State which parasite is depicted.
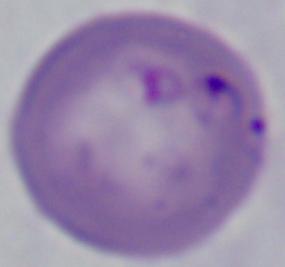
Babesia.

Micrograph. 1000x magnification.